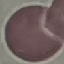
malaria status = uninfected
capture = smartphone through the microscope eyepiece
preparation = thin blood film
image type = automatically extracted cell patch, resized to 64 × 64 pixels
stain = Giemsa